Describe the morphology of the erythrocytes.
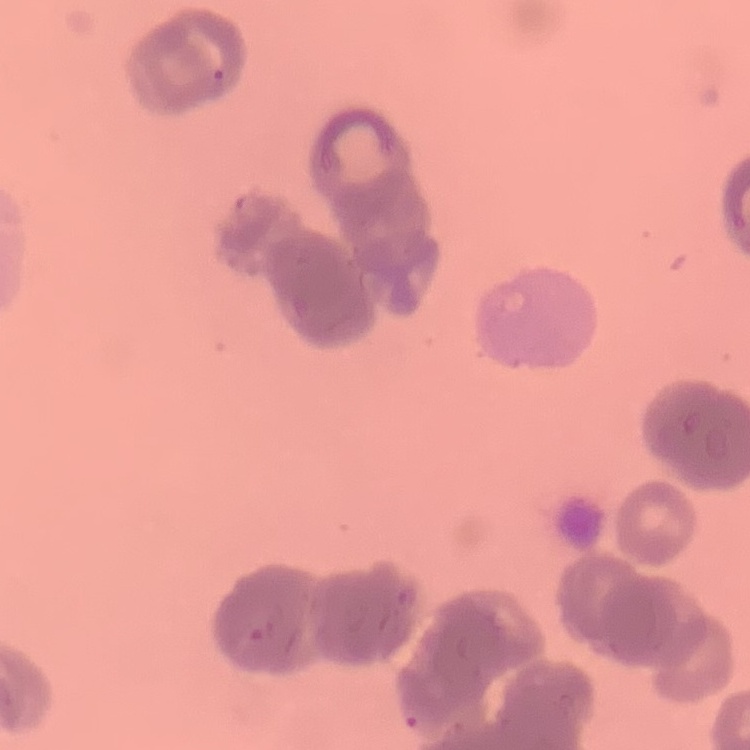
Rouleaux formation.

stain = Field's or Giemsa
preparation = thin blood film
image type = square crop of a larger photomicrograph